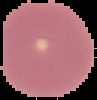

Summary:
  - Image size: 97×100 pixels
  - Image type: segmented cell region with the area outside set to black
  - Malaria status: uninfected
  - Preparation: thin blood smear